State which cell type is depicted.
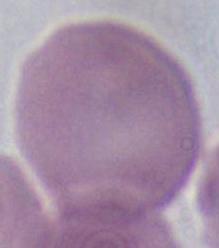

An erythrocyte.

modality = micrograph
magnification = 1000x